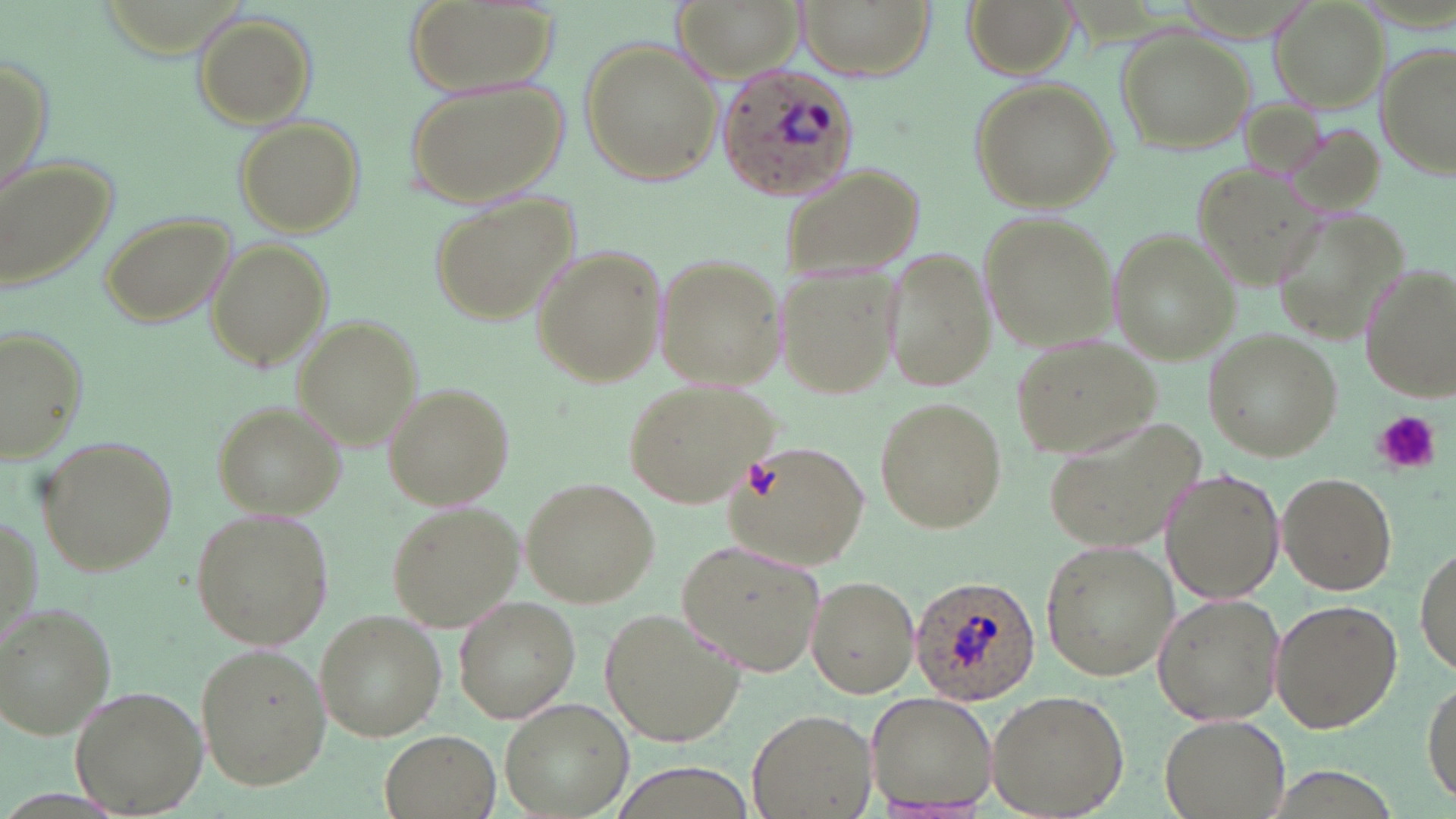
Plasmodium ovale-infected red blood cell locations = approximate bounding boxes as [x1, y1, x2, y2] in pixels: [716, 61, 860, 202], [908, 576, 1042, 708]
slide-level diagnosis = Plasmodium ovale
stain = May-Grünwald-Giemsa
preparation = thin blood smear
field of view = one of a larger specimen
magnification = 1000x
image size = 1456×819 pixels
platelet locations = approximate bounding boxes as [x1, y1, x2, y2] in pixels: [1375, 410, 1440, 474]
modality = optical microscopy
uninfected red blood cell locations = approximate bounding boxes as [x1, y1, x2, y2] in pixels: [401, 0, 566, 101], [678, 0, 806, 80], [795, 0, 933, 79], [961, 0, 1079, 78], [1270, 0, 1390, 111], [191, 11, 316, 126], [1118, 30, 1255, 152], [577, 39, 720, 186], [1375, 44, 1454, 181], [1, 47, 52, 195], [407, 76, 566, 207], [970, 79, 1116, 212], [237, 117, 365, 235], [1280, 120, 1389, 217], [0, 152, 119, 298], [1190, 161, 1324, 288], [777, 163, 925, 283], [430, 194, 575, 324], [1275, 208, 1412, 350], [99, 209, 237, 328], [978, 211, 1116, 350], [1107, 228, 1240, 362], [210, 238, 331, 371], [529, 243, 665, 388], [882, 246, 992, 394], [651, 249, 786, 389], [773, 262, 903, 400], [1357, 262, 1455, 401], [294, 317, 421, 448], [2, 326, 88, 463], [1203, 328, 1341, 461], [1008, 337, 1163, 461], [622, 375, 779, 508], [381, 382, 515, 511], [872, 397, 1007, 533], [214, 401, 343, 520], [1043, 417, 1210, 559], [37, 434, 179, 578], [721, 440, 869, 572], [1160, 466, 1285, 605], [1277, 472, 1396, 595], [523, 476, 662, 608], [385, 500, 520, 629], [192, 508, 336, 650], [675, 537, 827, 681], [1040, 538, 1178, 681], [1415, 539, 1455, 675], [806, 575, 916, 698], [1153, 593, 1284, 725], [452, 596, 581, 723], [1269, 598, 1403, 733], [0, 600, 117, 737], [316, 610, 445, 739], [600, 610, 745, 743], [191, 645, 332, 789], [1422, 673, 1456, 807], [72, 685, 203, 815], [985, 688, 1131, 819], [867, 691, 1001, 815], [502, 701, 630, 817], [750, 707, 875, 817], [1159, 713, 1292, 818], [379, 729, 499, 819]